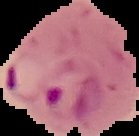

{
  "preparation": "thin blood film",
  "image_type": "cell region segmented out of the field of view; surrounding area masked to black",
  "result": "malaria parasites identified",
  "image_size": "139×136 pixels"
}